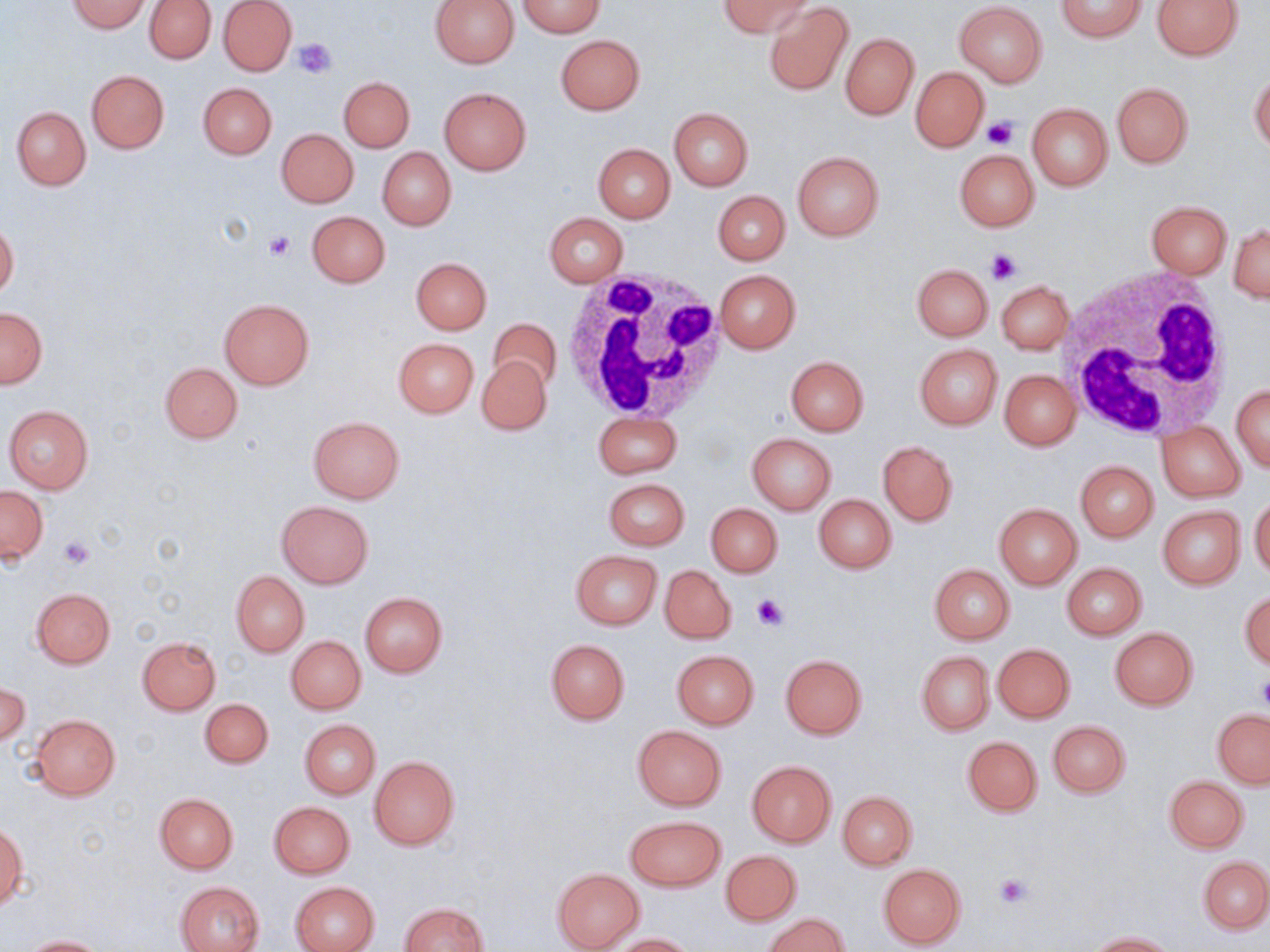
Approximate bounding boxes as (x1,y1)-(x2,y2) corner pairs in pixels. White blood cell locations: (1060,267)-(1237,441), (562,269)-(727,420). Uninfected red blood cell locations: (218,0)-(297,75), (430,0)-(521,69), (718,0)-(814,39), (1056,0)-(1145,42), (1152,0)-(1243,60), (68,1)-(150,33), (145,1)-(216,64), (516,1)-(604,37), (764,2)-(853,96), (955,2)-(1047,87), (840,33)-(918,120), (556,35)-(644,114), (911,68)-(989,152), (86,70)-(168,153), (1249,72)-(1270,153), (339,78)-(414,151), (198,82)-(276,159), (1112,83)-(1192,167), (439,88)-(531,174), (1026,103)-(1112,191), (11,106)-(91,190), (669,107)-(752,190), (276,128)-(359,207), (593,144)-(675,222), (378,147)-(455,230), (954,150)-(1039,231), (792,151)-(884,240), (713,190)-(789,264), (1146,201)-(1231,278), (308,210)-(391,288), (545,212)-(628,287), (0,222)-(18,298), (1229,222)-(1269,302), (411,257)-(491,334), (912,264)-(993,341), (714,269)-(801,353), (997,280)-(1074,354), (220,299)-(313,389), (0,307)-(47,388), (488,316)-(562,391), (393,338)-(478,417), (914,343)-(1002,429), (477,356)-(551,435), (785,356)-(869,436), (160,362)-(242,443), (999,369)-(1081,450), (1232,384)-(1270,472), (4,405)-(93,495), (593,411)-(681,478), (307,416)-(405,503), (1158,422)-(1245,501), (747,432)-(836,514), (878,441)-(957,525), (1075,460)-(1158,542), (604,478)-(689,549), (1,486)-(48,564), (814,493)-(896,574), (1250,496)-(1270,578), (276,501)-(373,587), (705,502)-(782,576), (994,503)-(1082,588), (1157,506)-(1246,588), (571,550)-(662,629), (1062,563)-(1147,639), (929,564)-(1014,643), (659,566)-(736,643), (231,570)-(309,655), (31,588)-(115,668), (1240,592)-(1270,670), (360,593)-(448,676), (1110,627)-(1198,709), (286,635)-(366,714), (137,636)-(220,714), (546,639)-(629,724), (993,643)-(1075,722), (672,650)-(758,729), (917,651)-(994,735), (780,653)-(867,739), (1,681)-(29,748), (200,698)-(272,768), (1213,710)-(1270,787), (29,714)-(121,800), (300,720)-(380,798), (1048,720)-(1130,797), (633,725)-(726,809), (963,736)-(1043,816), (368,755)-(459,849), (747,761)-(836,848), (1165,777)-(1249,852), (837,791)-(917,869), (154,793)-(238,873), (270,801)-(355,879), (625,816)-(724,891), (1,825)-(26,910), (720,849)-(802,926), (1199,856)-(1269,933), (878,864)-(965,948), (552,869)-(644,950), (176,880)-(265,952), (292,881)-(379,952), (399,902)-(489,952), (765,913)-(848,952), (1087,931)-(1177,951), (612,933)-(698,952), (20,936)-(107,952). Platelet locations: (292,39)-(335,78), (981,117)-(1017,149), (266,232)-(297,260), (985,248)-(1020,286), (57,536)-(95,570), (751,594)-(790,633), (1256,677)-(1270,712), (995,872)-(1030,908). Slide-level diagnosis: no evidence of blood parasites. Image is 1270×952 pixels. Captured at 1000x magnification. Light microscopy. Thin blood smear. One field of a larger specimen. May-Grünwald-Giemsa stain.